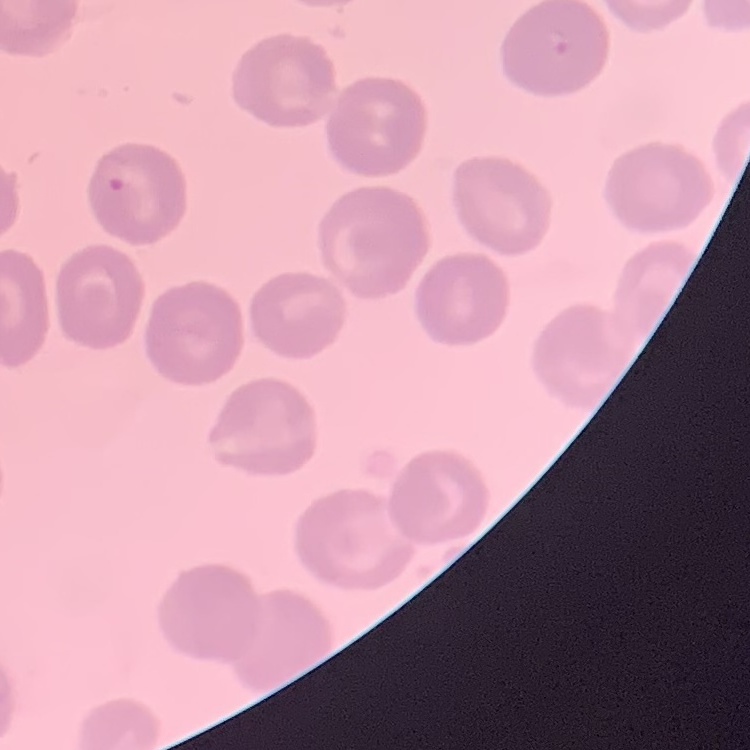
Summary:
  - Erythrocyte morphology: no rouleaux formation
  - Image type: one tile cut from a larger photomicrograph
  - Stain: Field's or Giemsa
  - Preparation: thin peripheral smear